State which cell type is depicted.
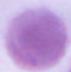

An erythrocyte.

modality = photomicrograph
magnification = 1000x